Give the extent of all Plasmodium ovale-infected red blood cells.
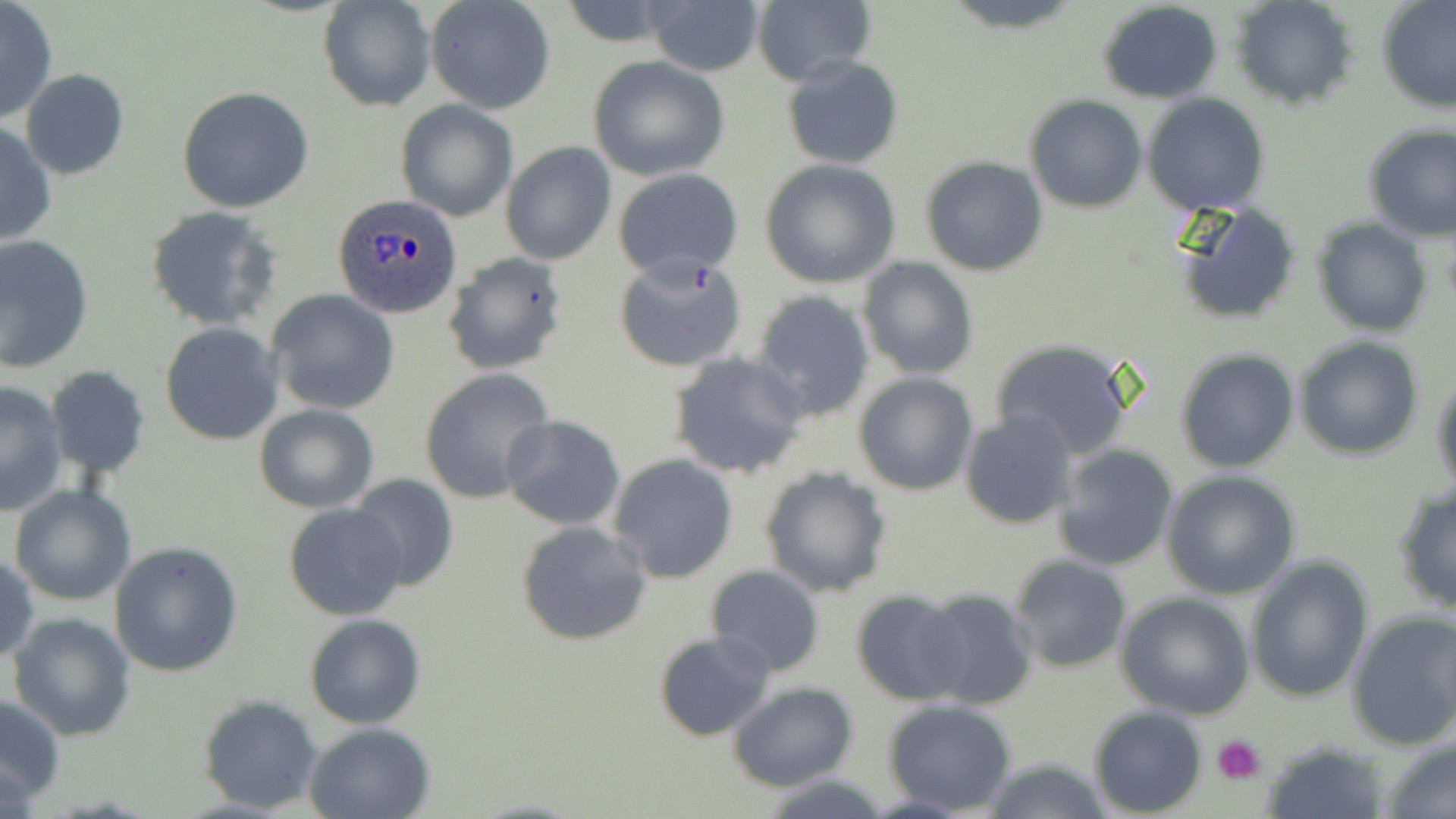

Approximate bounding boxes as [x1, y1, x2, y2] in pixels.
Plasmodium ovale-infected red blood cells: [331, 193, 463, 320].

slide_level_diagnosis: Plasmodium ovale
stain: May-Grünwald-Giemsa
image_size: 1456×819 pixels
platelet_locations: 'approximate bounding boxes as [x1, y1, x2, y2] in pixels: [1213, 734, 1266, 784]'
field_of_view: single
preparation: thin blood smear
modality: optical microscopy
uninfected_red_blood_cell_locations: 'approximate bounding boxes as [x1, y1, x2, y2] in pixels: [0, 0, 58, 124], [317, 0, 434, 112], [425, 0, 556, 114], [940, 0, 1087, 32], [1231, 0, 1359, 110], [1377, 1, 1456, 114], [647, 2, 764, 77], [751, 2, 875, 87], [1095, 2, 1224, 105], [783, 54, 904, 170], [587, 55, 730, 181], [21, 70, 129, 181], [175, 86, 315, 213], [1142, 93, 1270, 216], [1025, 95, 1147, 213], [396, 100, 519, 220], [0, 121, 55, 248], [1363, 123, 1456, 240], [500, 141, 616, 266], [921, 156, 1049, 276], [758, 159, 902, 288], [613, 169, 744, 280], [1167, 197, 1303, 325], [144, 207, 281, 331], [1312, 219, 1433, 336], [0, 235, 95, 373], [442, 252, 567, 376], [612, 253, 747, 373], [858, 258, 978, 381], [267, 289, 400, 415], [751, 289, 875, 423], [160, 323, 283, 446], [1294, 336, 1423, 459], [989, 338, 1138, 459], [1175, 348, 1300, 473], [669, 352, 810, 480], [45, 365, 150, 478], [420, 368, 554, 505], [1431, 369, 1455, 500], [853, 373, 978, 495], [0, 380, 69, 516], [253, 403, 378, 513], [960, 409, 1077, 531], [501, 416, 626, 530], [1052, 444, 1181, 571], [608, 454, 737, 584], [759, 466, 891, 598], [1162, 470, 1301, 598], [348, 472, 461, 593], [1391, 481, 1456, 615], [10, 484, 137, 605], [285, 502, 410, 621], [515, 520, 652, 647], [109, 542, 243, 678], [0, 553, 38, 665], [1006, 555, 1132, 674], [1244, 557, 1374, 704], [705, 565, 825, 677], [914, 588, 1039, 711], [851, 589, 970, 707], [1117, 592, 1256, 719], [1346, 610, 1456, 750], [8, 612, 136, 740], [304, 613, 427, 729], [652, 630, 779, 743], [728, 681, 857, 791], [1, 693, 66, 806], [198, 694, 325, 814], [881, 698, 1017, 815], [1088, 708, 1209, 817], [304, 722, 438, 818], [1259, 739, 1389, 818], [1379, 740, 1456, 819], [977, 759, 1116, 818], [761, 774, 893, 817]'
magnification: 1000x